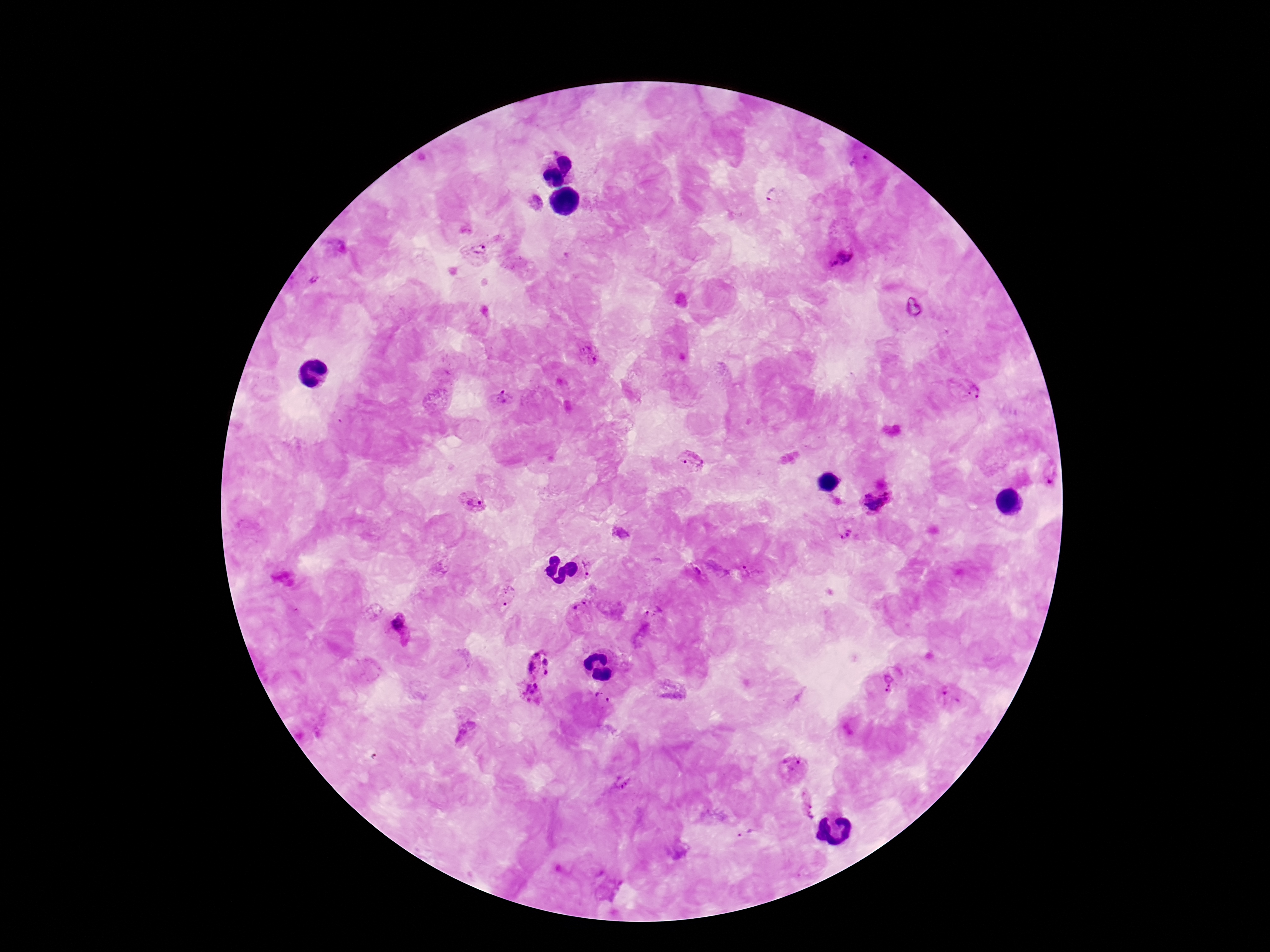

Approximate centers as {x, y} in pixels. Plasmodium parasite locations: {860, 162}, {775, 196}, {536, 201}, {478, 250}, {843, 258}, {312, 282}, {588, 353}, {971, 393}, {500, 397}, {689, 462}, {1050, 478}, {877, 500}, {472, 502}, {846, 533}, {620, 534}, {593, 565}, {754, 571}, {506, 595}, {579, 608}, {652, 610}, {400, 626}, {540, 665}, {888, 682}, {943, 692}, {527, 693}, {603, 697}, {466, 730}, {794, 766}, {623, 782}, {807, 804}, {749, 834}. 100x magnification. Single field of view. Giemsa stain. Patient malaria status: infected. Thick peripheral-blood smear. Smartphone photograph taken through the microscope eyepiece. Image is 1270×952 pixels.